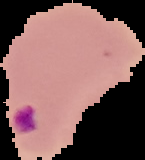 Result: Plasmodium parasites detected. Image is 145×160 pixels. The area outside the segmented cell region is set to black. From a thin blood film.